Report the malaria status of this cell.
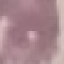

It is uninfected.

Summary:
  - Image type: automatically extracted cell patch, resized to 64 × 64 pixels
  - Capture: smartphone camera at the microscope eyepiece
  - Preparation: thin blood smear
  - Stain: Giemsa